Name the parasite shown.
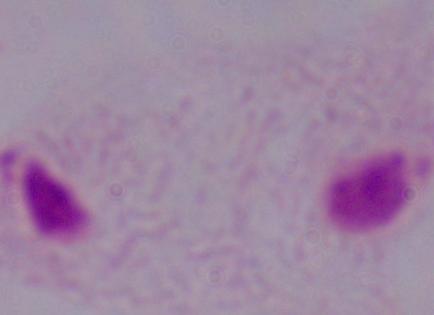

This is a trichomonad.

Captured at 1000x magnification. Photomicrograph.